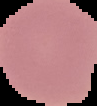

Summary:
  - Image type: cell region segmented out of the field of view; surrounding area masked to black
  - Preparation: thin blood film
  - Image size: 97×106 pixels
  - Malaria status: uninfected